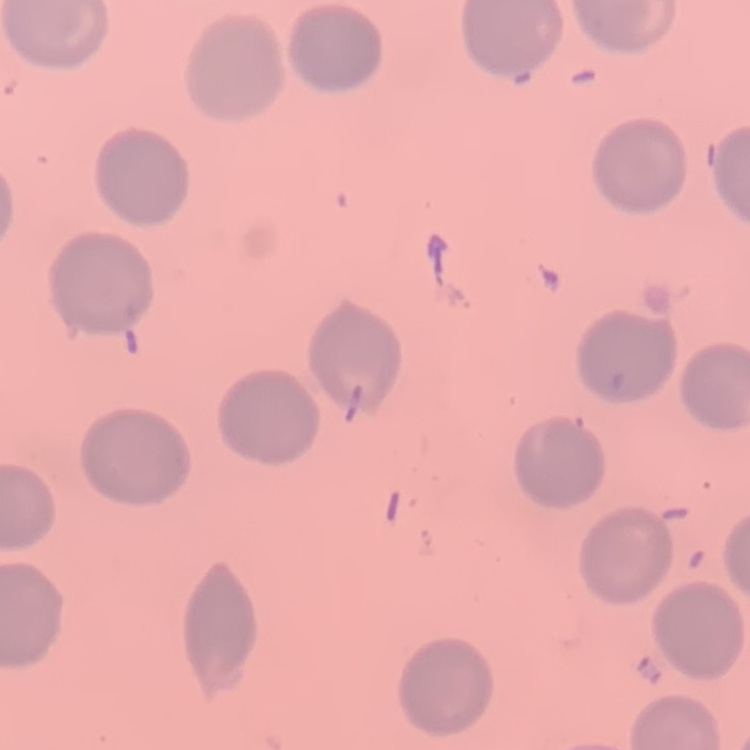
Summary:
  - Erythrocyte morphology: no rouleaux formation
  - Preparation: thin blood smear
  - Image type: one tile cut from a larger photomicrograph
  - Stain: Field's or Giemsa